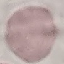
Result: no malaria parasites seen. Thin blood smear. Photographed with a smartphone camera at the microscope eyepiece. Cell patch, automatically extracted from a larger field of view and resized to 64 × 64 pixels. Giemsa-stained preparation.